Identify the preparation type.
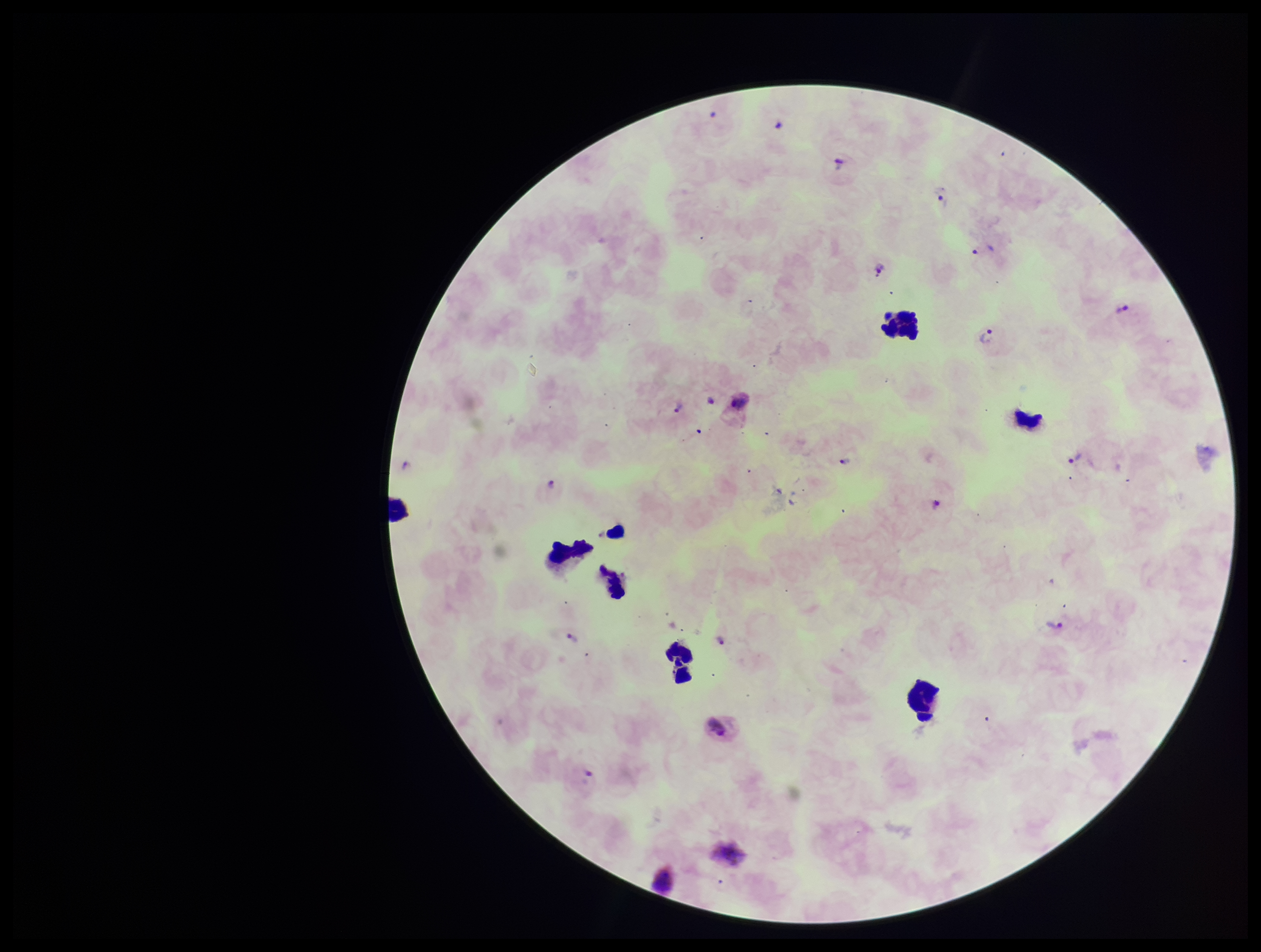
Thick.

One field from this slide. Parasite count: 11. Patient malaria status: infected. Image is 1261×952 pixels. Stained with Giemsa. Plasmodium parasites: identified. Smartphone photograph taken through the eyepiece of a microscope. Leukocyte count: 6. Species reported for this patient: Plasmodium vivax.